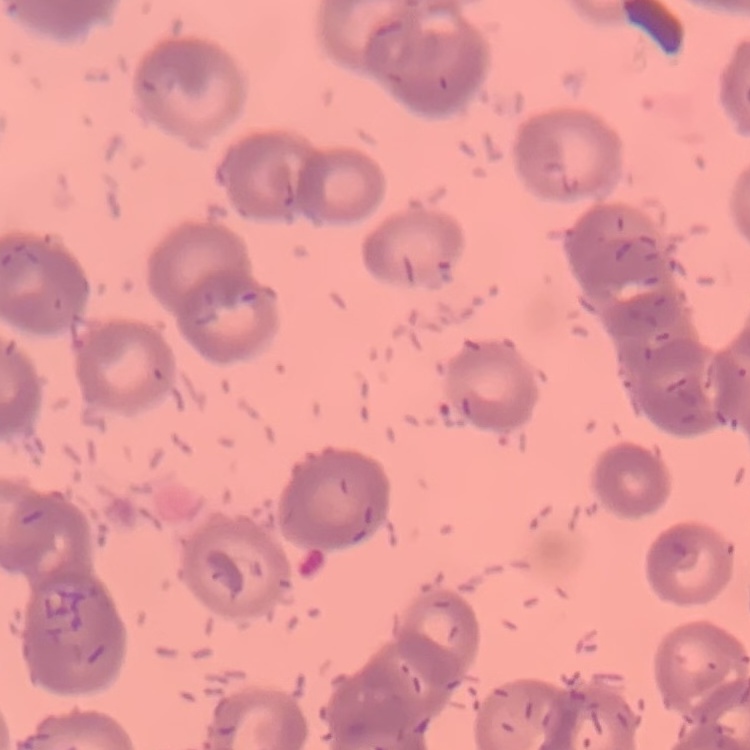
erythrocyte morphology = rouleaux formation
image type = one tile cut from a larger photomicrograph
preparation = thin blood film
stain = Field's or Giemsa